Assess this cell for malaria.
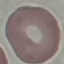

Uninfected.

stain: Giemsa
capture: smartphone camera at the microscope eyepiece
image_type: automatically extracted cell patch, resized to 64 × 64 pixels
preparation: thin smear